Classify this cell by malaria status.
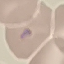
Uninfected.

preparation = thin smear
stain = Giemsa
image type = cell patch, automatically extracted from a larger field of view and resized to 64 × 64 pixels
capture = smartphone through the microscope eyepiece